Outline each uninfected red blood cell.
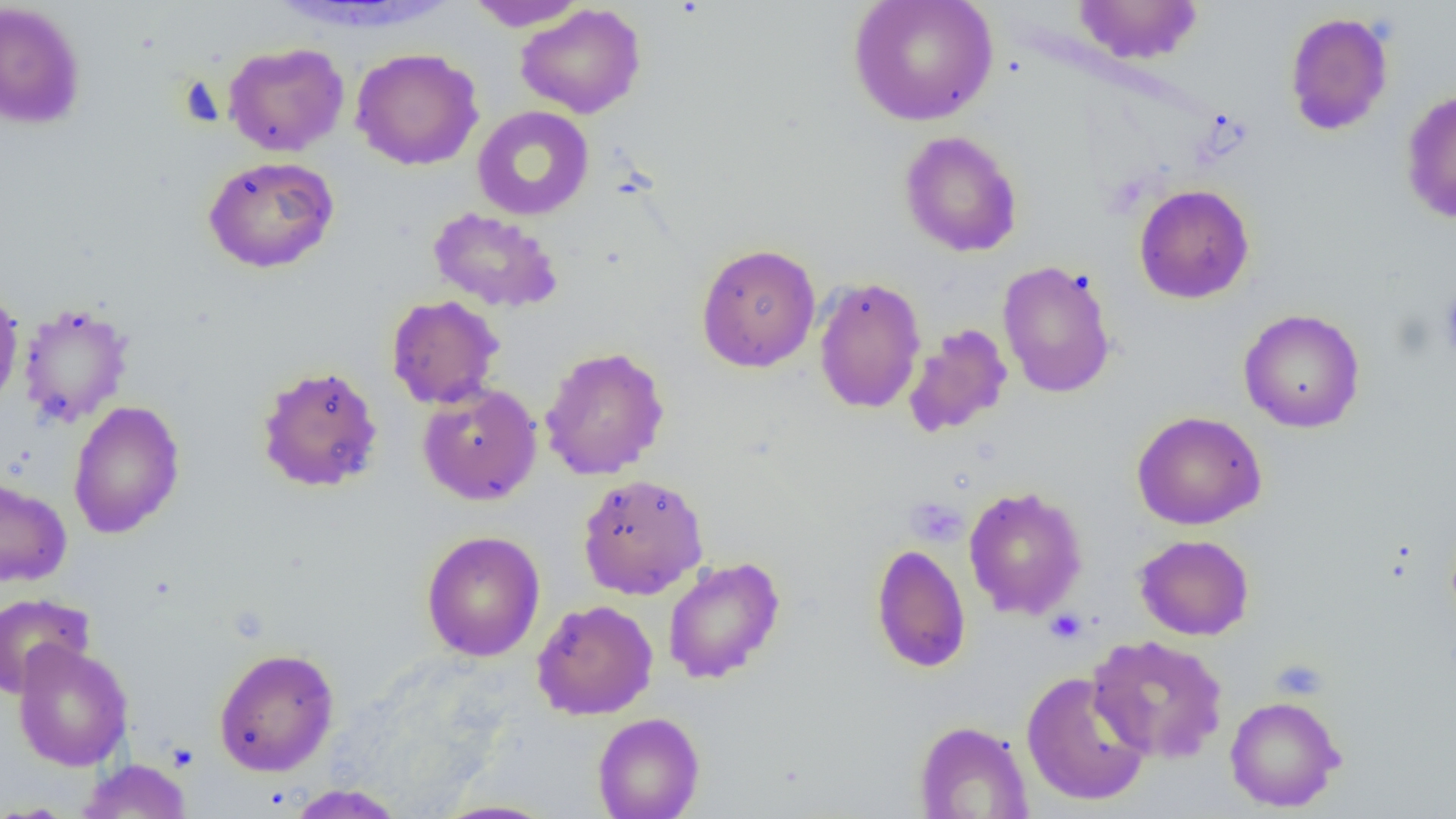

Approximate bounding boxes as (x1,y1)-(x2,y2) corner pairs in pixels.
Uninfected red blood cells: (464,0)-(587,30), (847,0)-(998,127), (1072,0)-(1203,64), (0,1)-(86,130), (515,3)-(646,119), (1284,11)-(1394,136), (223,42)-(349,157), (350,48)-(484,171), (1400,89)-(1456,225), (472,105)-(595,221), (898,130)-(1023,257), (203,155)-(340,273), (1133,184)-(1255,304), (427,207)-(563,313), (695,243)-(821,373), (997,260)-(1117,398), (813,276)-(926,414), (0,284)-(24,411), (385,294)-(504,409), (18,303)-(134,428), (1238,308)-(1365,433), (903,323)-(1013,438), (539,346)-(670,480), (255,364)-(384,494), (416,377)-(672,493), (417,382)-(543,506), (67,399)-(185,539), (1131,410)-(1266,530), (577,473)-(709,600), (0,475)-(72,587), (964,486)-(1087,620), (421,530)-(545,661), (1134,534)-(1254,640), (871,543)-(971,673), (662,557)-(785,684), (0,593)-(94,698), (532,599)-(658,720), (1087,634)-(1229,763), (12,641)-(134,771), (213,647)-(340,777), (1021,671)-(1152,806), (1224,695)-(1345,812), (592,712)-(705,819), (913,720)-(1034,818), (78,759)-(193,818), (286,784)-(407,818), (430,799)-(561,818).

Summary:
  - Platelet locations: (905,496)-(967,546), (1045,609)-(1087,644), (1270,658)-(1329,700)
  - Slide-level diagnosis: negative for blood parasites
  - Preparation: thin blood smear
  - Field of view: single
  - Magnification: 1000x
  - Image size: 1456×819 pixels
  - Modality: light microscopy